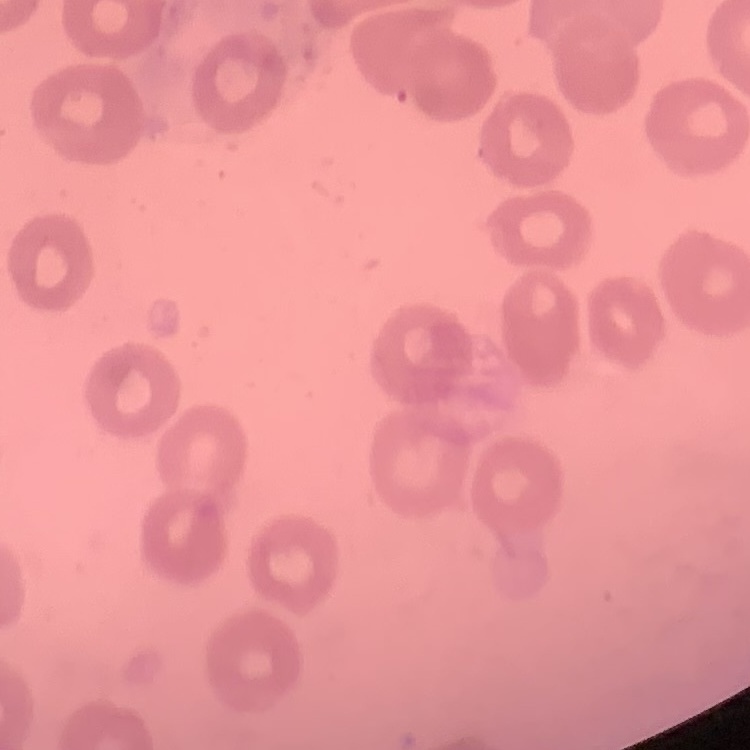
{
  "erythrocyte_morphology": "no rouleaux formation",
  "stain": "Field's or Giemsa",
  "image_type": "square crop of a larger photomicrograph",
  "preparation": "thin blood film"
}